Name the cell type shown.
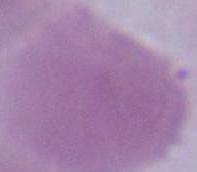

An erythrocyte.

Summary:
  - Modality: micrograph
  - Magnification: 1000x